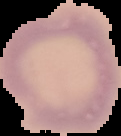
result: no malaria parasites seen
image_type: segmented cell region with the area outside set to black
image_size: 121×136 pixels
preparation: thin blood smear